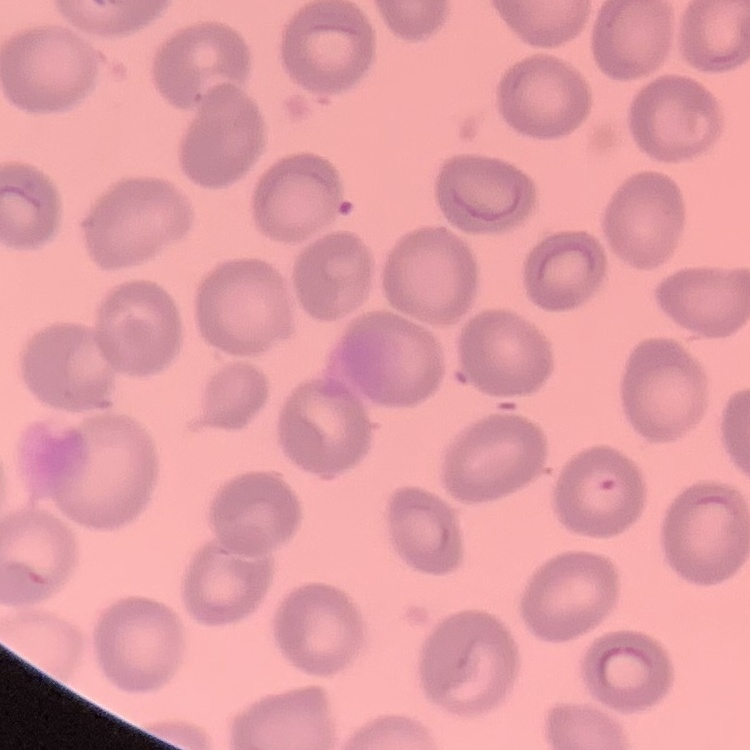

red blood cell morphology = no rouleaux formation
image type = square crop of a larger photomicrograph
stain = Field's or Giemsa
preparation = thin peripheral smear